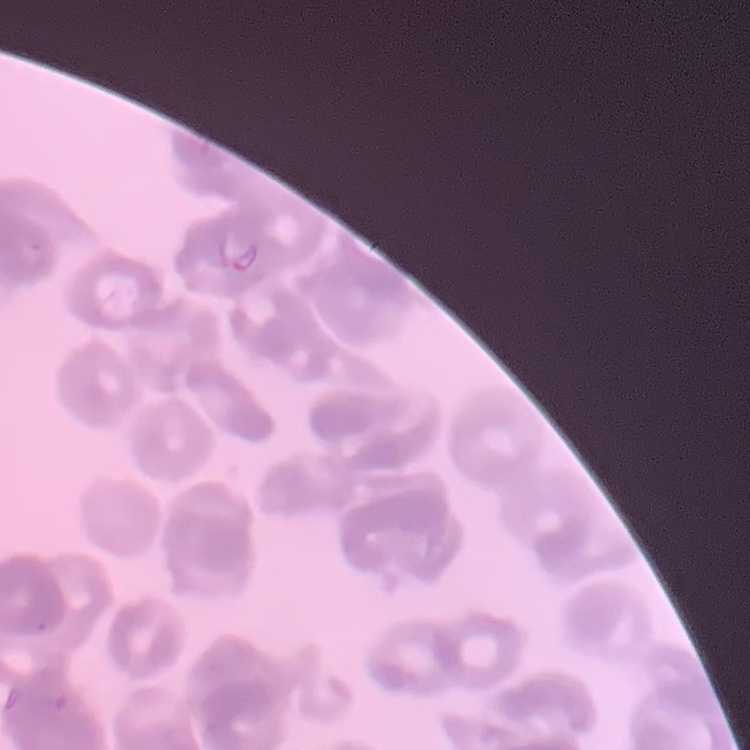

red_blood_cell_morphology: rouleaux formation
preparation: thin blood smear
stain: Field's or Giemsa
image_type: square crop of a larger photomicrograph